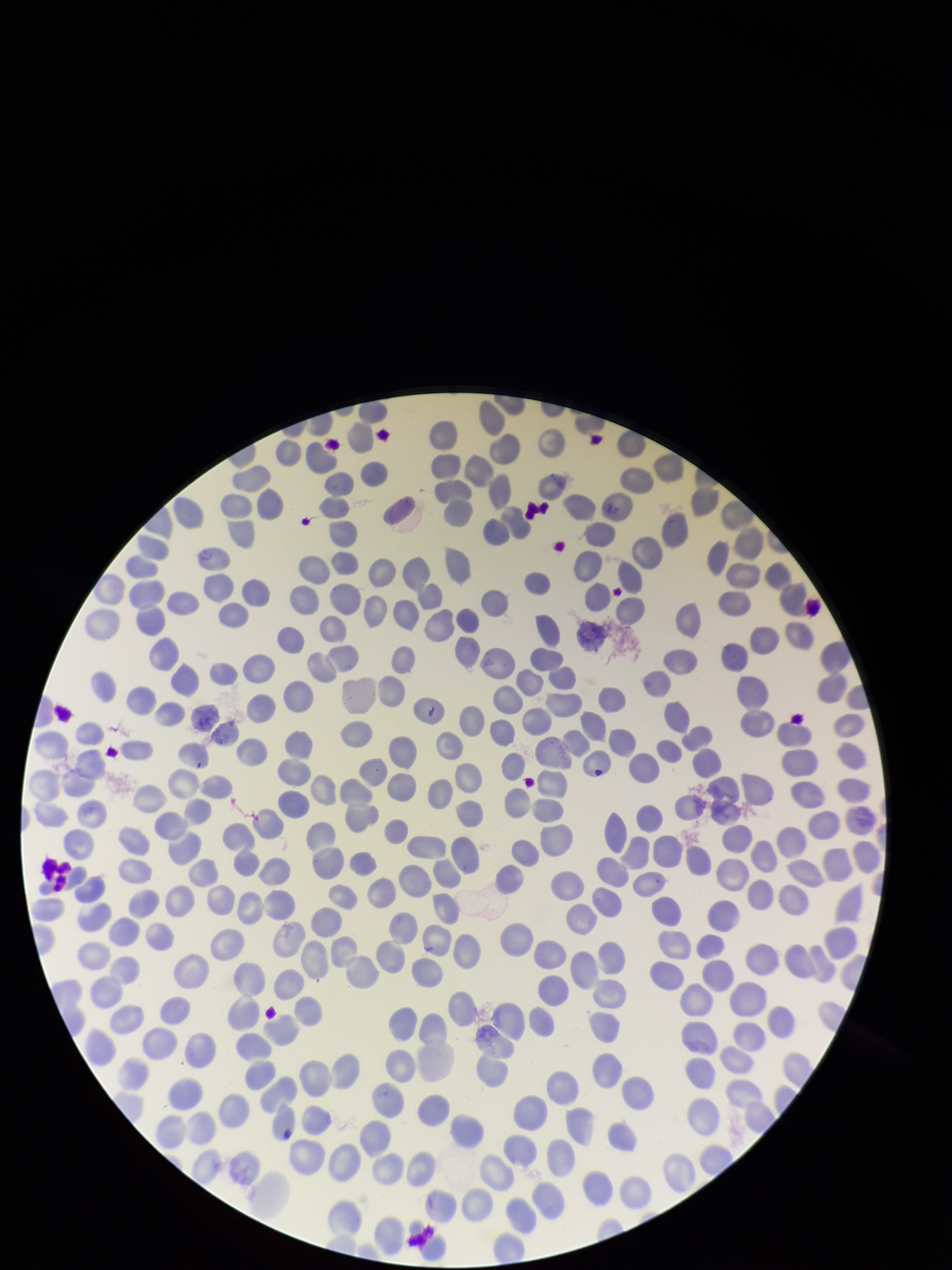

field of view = single
stain = Giemsa
red blood cell count = 241
parasitized red blood cell count = 0
capture = smartphone photograph through the microscope eyepiece
parasitized red blood cells = none detected
patient malaria status = negative
image size = 952×1270 pixels
preparation = thin blood smear